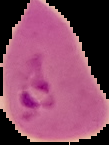
preparation = thin blood smear
image type = segmented cell region on a black background
image size = 109×145 pixels
result = Plasmodium parasites identified